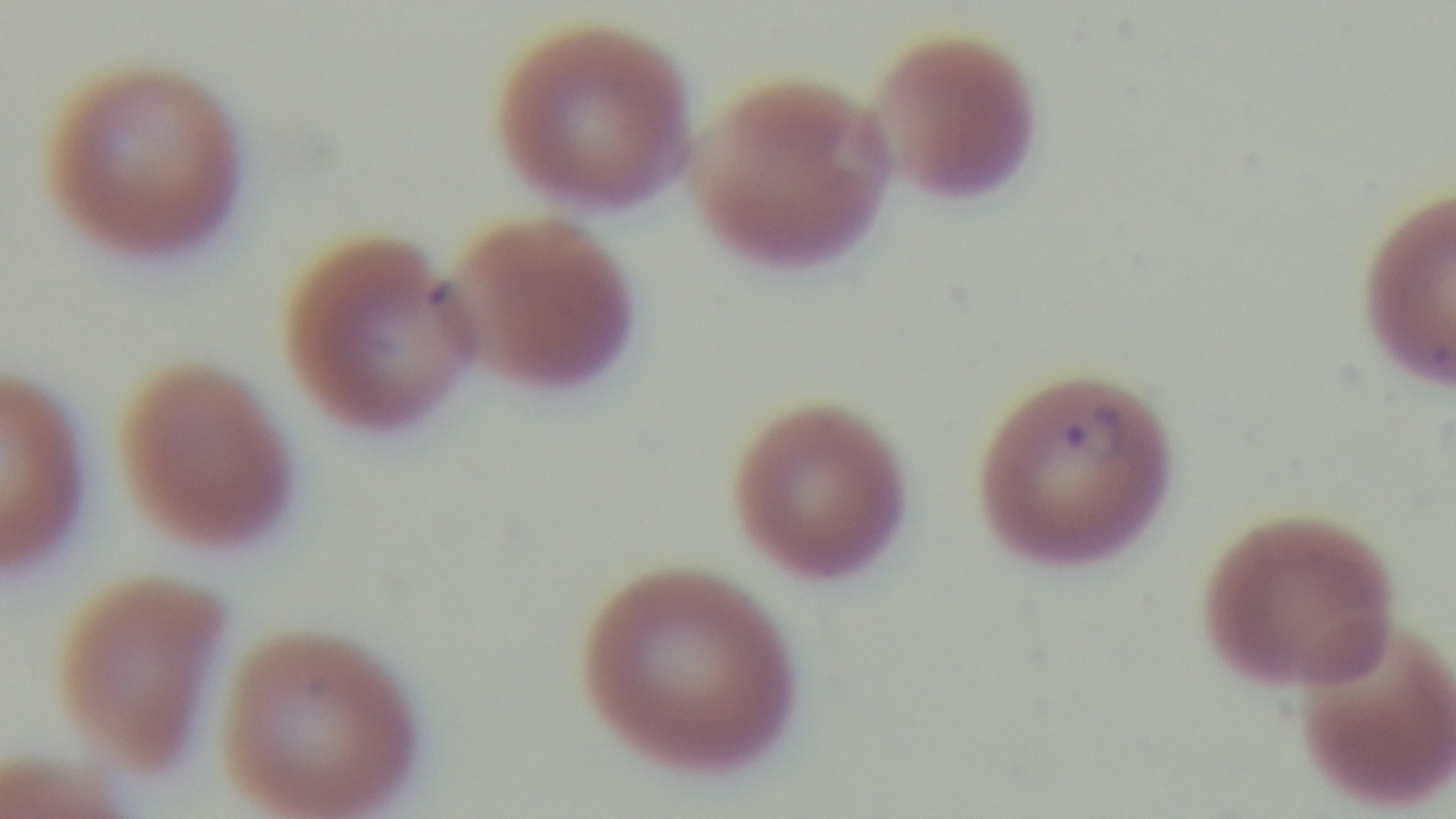
Summary:
  - Objective: 100x oil immersion
  - Preparation: thin
  - Modality: light microscopy
  - Field of view: single
  - Stain: Giemsa
  - Malaria status: positive
  - Capture: mounted 4K digital camera